Outline each uninfected red blood cell.
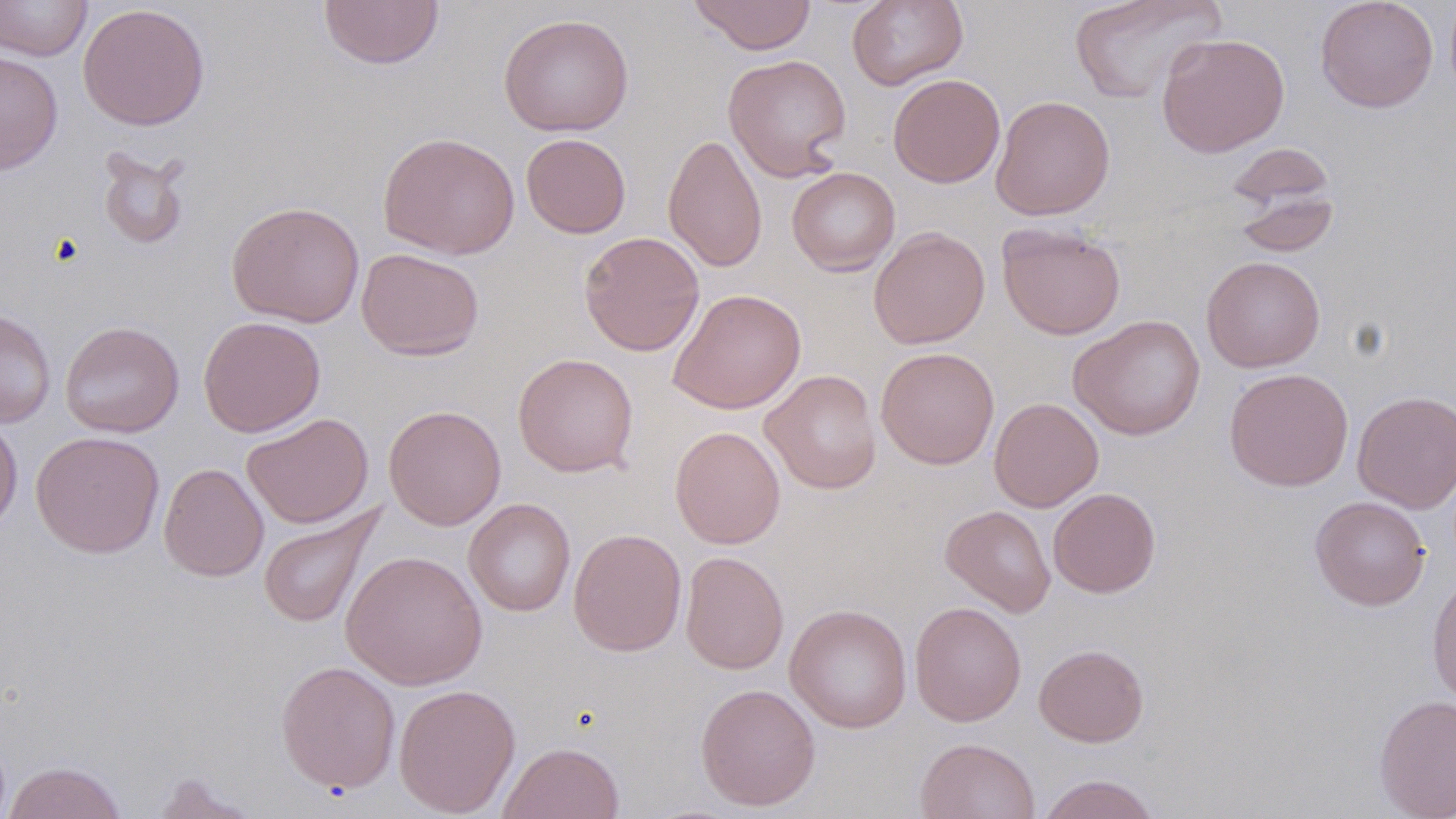
Approximate bounding boxes as (x1, y1, x2, y2) in pixels.
Uninfected red blood cells: (0, 0, 93, 61), (318, 0, 444, 70), (687, 0, 818, 55), (847, 0, 968, 90), (1068, 0, 1226, 104), (1314, 0, 1438, 113), (78, 2, 210, 131), (498, 13, 634, 136), (1156, 32, 1290, 158), (0, 51, 64, 175), (723, 54, 852, 181), (888, 73, 1005, 188), (990, 95, 1115, 220), (377, 132, 520, 260), (521, 133, 632, 238), (663, 133, 767, 273), (1224, 142, 1337, 211), (96, 147, 191, 252), (787, 166, 900, 276), (1231, 190, 1340, 258), (226, 201, 365, 328), (997, 222, 1126, 340), (868, 226, 990, 349), (578, 231, 705, 356), (357, 247, 484, 360), (1201, 255, 1326, 373), (667, 288, 806, 414), (0, 307, 56, 428), (1068, 314, 1206, 440), (198, 315, 326, 437), (60, 321, 184, 438), (875, 346, 1000, 469), (513, 353, 639, 477), (1223, 367, 1354, 491), (760, 369, 882, 494), (1352, 390, 1456, 513), (988, 397, 1104, 513), (383, 404, 506, 530), (242, 412, 374, 529), (0, 415, 23, 536), (669, 426, 786, 549), (30, 430, 165, 558), (158, 463, 268, 581), (1048, 487, 1161, 598), (1310, 496, 1430, 610), (463, 498, 576, 617), (940, 505, 1056, 616), (259, 506, 380, 629), (568, 528, 687, 657), (340, 550, 488, 690), (680, 551, 789, 674), (1427, 571, 1456, 709), (909, 601, 1027, 726), (785, 604, 912, 733), (1033, 644, 1149, 747), (276, 660, 401, 794), (393, 683, 520, 817), (695, 683, 821, 811), (1374, 694, 1456, 819), (915, 737, 1040, 819), (497, 742, 625, 819), (3, 760, 127, 819), (148, 771, 259, 818), (1036, 774, 1161, 819).

{
  "slide_level_diagnosis": "no evidence of blood parasites",
  "image_size": "1456×819 pixels",
  "field_of_view": "one of a larger specimen",
  "magnification": "1000x",
  "stain": "May-Grünwald-Giemsa",
  "modality": "light microscopy",
  "preparation": "thin blood film"
}